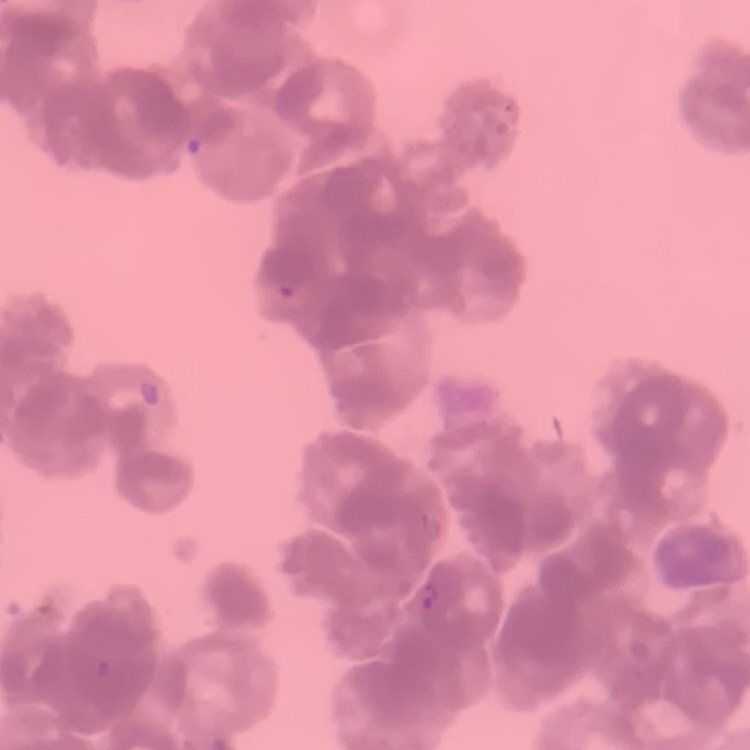

Summary:
  - Erythrocyte morphology: rouleaux formation
  - Image type: square crop of a larger photomicrograph
  - Stain: Field's or Giemsa
  - Preparation: thin blood film